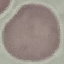
Malaria status: uninfected. Giemsa-stained preparation. Automatically extracted cell patch, resized to 64 × 64 pixels. Photographed with a smartphone camera at the microscope eyepiece. Thin smear of blood.